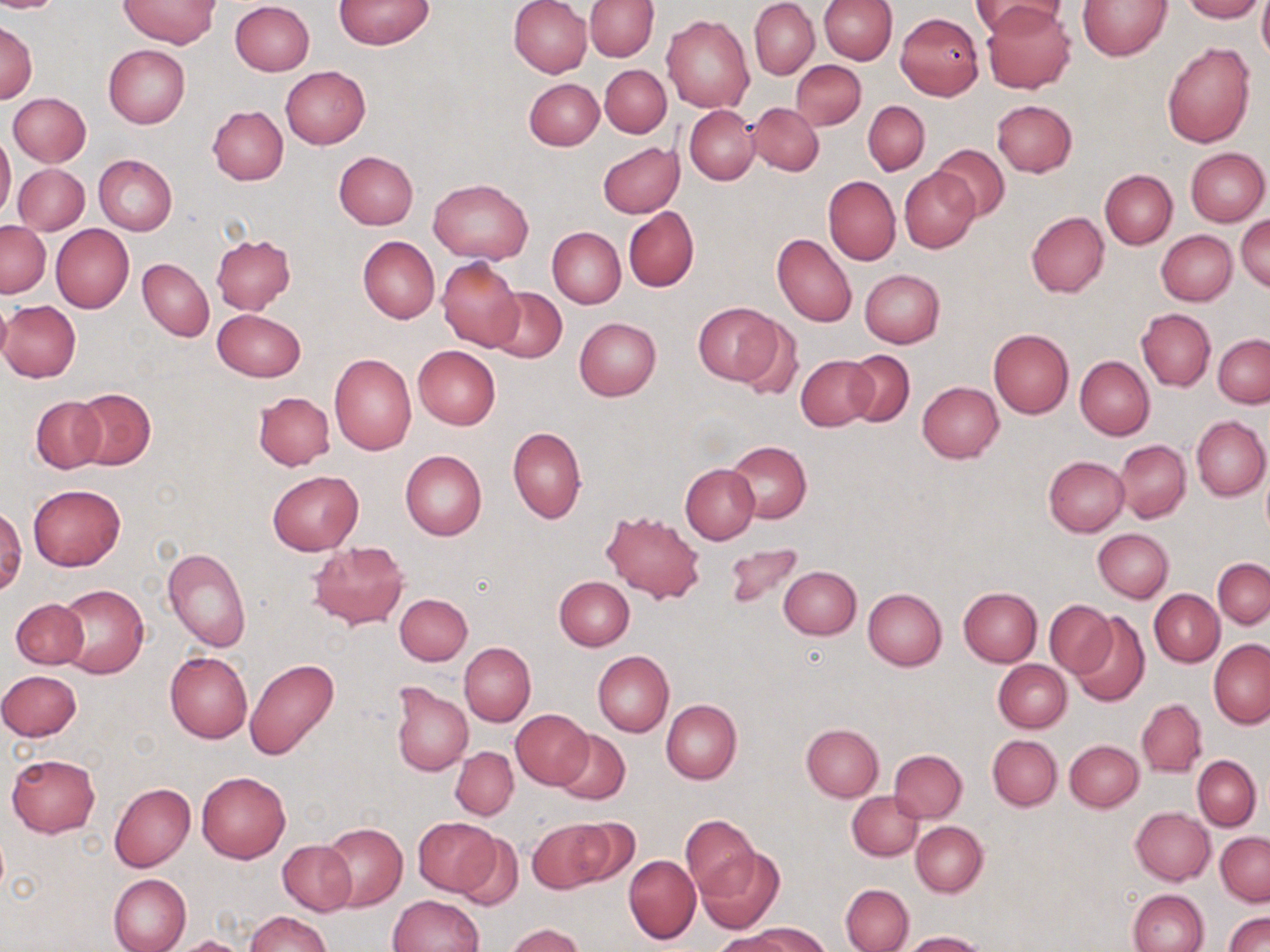
Approximate bounding boxes as [x1, y1, x2, y2] in pixels. Uninfected red blood cell locations: [0, 0, 63, 12], [121, 0, 220, 48], [335, 0, 434, 50], [509, 0, 591, 78], [585, 0, 659, 61], [750, 0, 819, 80], [818, 0, 896, 63], [971, 0, 1068, 39], [1078, 0, 1173, 60], [1182, 0, 1264, 22], [1257, 0, 1270, 62], [230, 1, 314, 76], [982, 3, 1075, 94], [895, 12, 984, 99], [662, 15, 754, 114], [1, 20, 36, 104], [1161, 42, 1255, 147], [104, 45, 190, 128], [791, 60, 865, 129], [600, 65, 671, 137], [280, 66, 371, 149], [524, 79, 604, 151], [8, 93, 91, 166], [993, 100, 1077, 177], [863, 101, 929, 175], [748, 103, 824, 176], [208, 106, 288, 185], [685, 106, 758, 185], [0, 131, 16, 219], [597, 141, 684, 218], [931, 144, 1009, 220], [1185, 147, 1268, 225], [334, 151, 418, 230], [94, 154, 177, 234], [13, 163, 89, 234], [899, 168, 980, 252], [1100, 170, 1177, 249], [824, 177, 900, 264], [428, 178, 533, 263], [623, 207, 699, 291], [1026, 211, 1109, 297], [1237, 216, 1269, 292], [1, 221, 49, 297], [51, 224, 134, 312], [548, 227, 625, 308], [1157, 230, 1237, 305], [772, 233, 857, 327], [212, 235, 295, 314], [359, 236, 440, 323], [437, 257, 523, 352], [138, 258, 213, 341], [859, 269, 945, 348], [486, 286, 567, 363], [0, 298, 11, 370], [1, 300, 81, 382], [693, 301, 784, 386], [213, 309, 306, 382], [1137, 309, 1215, 390], [733, 314, 803, 399], [574, 317, 661, 401], [988, 330, 1073, 418], [1213, 334, 1270, 408], [413, 345, 500, 430], [845, 350, 914, 426], [329, 353, 417, 455], [796, 355, 877, 431], [1075, 356, 1155, 440], [917, 380, 1004, 463], [72, 388, 155, 471], [253, 392, 335, 471], [32, 396, 105, 473], [1192, 416, 1270, 502], [508, 426, 586, 523], [727, 440, 811, 522], [1114, 440, 1193, 522], [400, 450, 487, 541], [1043, 455, 1128, 536], [679, 464, 759, 543], [1261, 465, 1270, 540], [267, 470, 363, 556], [27, 484, 126, 572], [0, 506, 24, 596], [602, 510, 705, 602], [1091, 528, 1173, 602], [306, 540, 410, 630], [723, 545, 804, 610], [162, 547, 251, 652], [1212, 558, 1269, 629], [779, 565, 861, 638], [553, 576, 635, 650], [54, 584, 149, 679], [958, 587, 1042, 666], [863, 589, 947, 670], [1150, 590, 1223, 666], [393, 593, 473, 665], [11, 598, 89, 668], [1045, 600, 1114, 678], [1068, 611, 1151, 708], [1209, 640, 1270, 728], [459, 643, 535, 727], [165, 651, 253, 743], [592, 651, 673, 736], [244, 658, 339, 762], [994, 659, 1071, 731], [1, 670, 82, 740], [390, 682, 473, 776], [662, 699, 741, 784], [1137, 699, 1206, 776], [512, 710, 592, 789], [801, 723, 884, 800], [553, 728, 630, 805], [988, 735, 1062, 810], [1064, 740, 1144, 811], [450, 746, 518, 820], [888, 749, 967, 822], [6, 753, 100, 837], [1192, 755, 1262, 830], [196, 771, 291, 863], [109, 783, 195, 872], [847, 791, 922, 860], [1131, 807, 1214, 885], [679, 815, 760, 899], [413, 817, 499, 895], [564, 819, 642, 887], [530, 820, 616, 892], [911, 821, 987, 897], [321, 823, 407, 911], [451, 830, 524, 911], [1217, 832, 1269, 905], [278, 841, 356, 916], [697, 846, 785, 933], [624, 855, 700, 944], [108, 873, 191, 952], [841, 883, 914, 952], [1128, 889, 1209, 952], [388, 895, 485, 951], [245, 911, 329, 952], [1224, 911, 1270, 951], [505, 923, 583, 952], [741, 924, 831, 952], [713, 930, 796, 952], [902, 930, 987, 952], [174, 936, 251, 952]. Slide-level diagnosis: negative for blood parasites. Image is 1270×952 pixels. Captured at 1000x magnification. One field of a larger specimen. May-Grünwald-Giemsa-stained preparation. Light microscopy. Thin blood film.